Identify the cell.
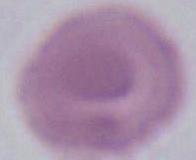

This is an erythrocyte.

Captured at 1000x magnification. Photomicrograph.